Classify this cell by malaria status.
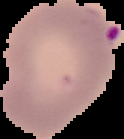
It is parasitized.

image_size: 124×139 pixels
preparation: thin blood film
image_type: segmented cell region on a black background